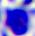
Micrograph. A leukocyte is seen. Captured at 400x magnification.